Assess this cell for malaria.
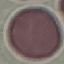

It is uninfected.

Automatically extracted cell patch, resized to 64 × 64 pixels. Giemsa-stained preparation. Acquired by smartphone through the microscope eyepiece. Thin blood smear.